Describe the morphology of the red blood cells.
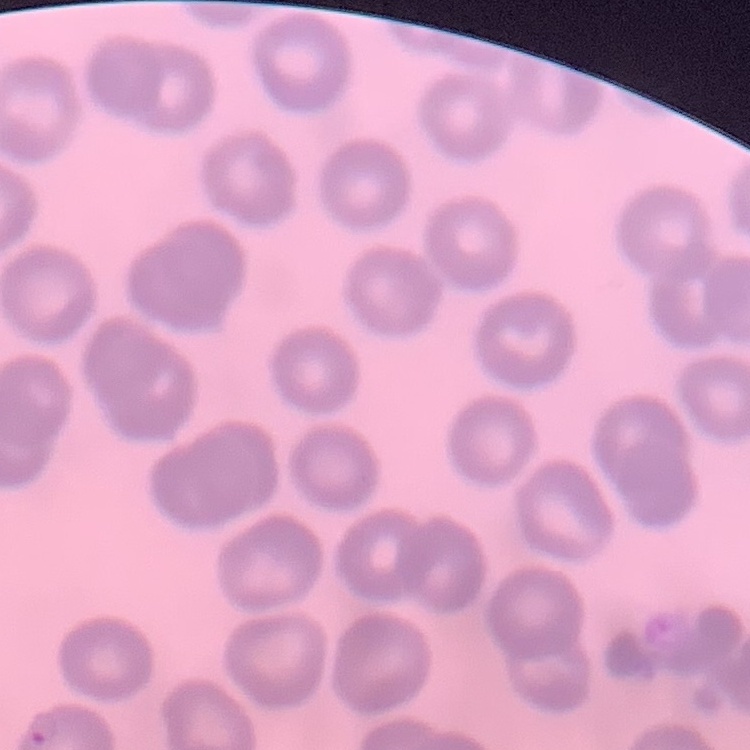

No rouleaux formation.

Field's or Giemsa stain. Thin blood film. Square crop of a larger photomicrograph.